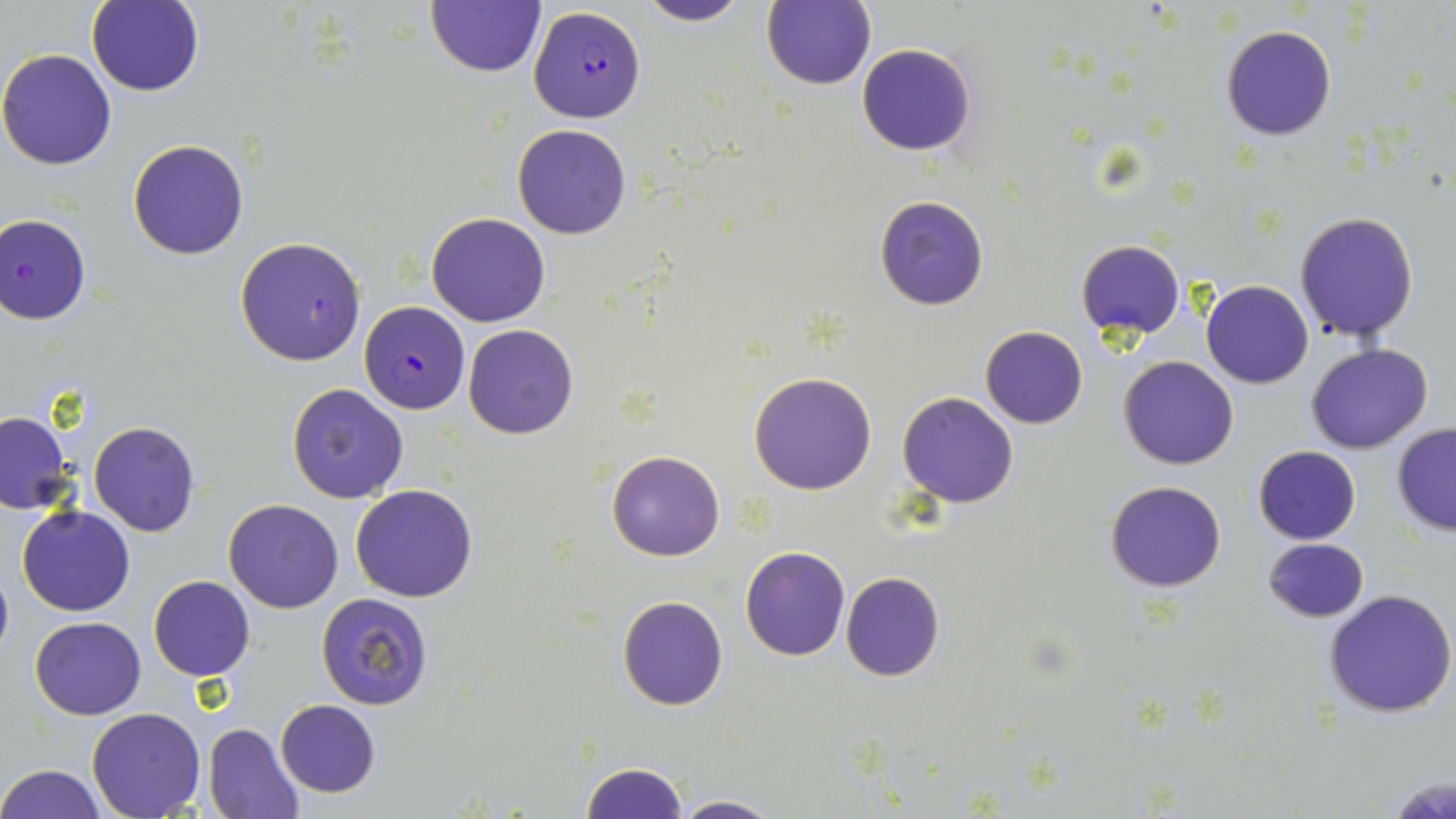

{
  "slide_level_diagnosis": "Plasmodium falciparum",
  "modality": "optical microscopy",
  "magnification": "1000x",
  "image_size": "1456×819 pixels",
  "preparation": "thin blood film",
  "plasmodium_falciparum_infected_red_blood_cell_locations": "approximate bounding boxes as [x1, y1, x2, y2] in pixels: [527, 5, 645, 124], [0, 213, 91, 323], [234, 236, 367, 367], [360, 300, 469, 412]",
  "uninfected_red_blood_cell_locations": "approximate bounding boxes as [x1, y1, x2, y2] in pixels: [86, 0, 205, 96], [636, 0, 753, 26], [424, 1, 545, 78], [760, 1, 876, 90], [1220, 24, 1337, 140], [856, 43, 978, 157], [0, 47, 119, 170], [512, 124, 632, 240], [128, 137, 251, 260], [874, 195, 990, 311], [1294, 210, 1420, 341], [427, 212, 548, 326], [1076, 240, 1186, 341], [1201, 280, 1314, 389], [463, 323, 579, 439], [980, 326, 1088, 429], [1306, 343, 1433, 455], [1118, 355, 1239, 470], [749, 371, 878, 495], [286, 384, 410, 503], [898, 392, 1019, 508], [0, 411, 73, 514], [88, 421, 201, 537], [1391, 423, 1456, 536], [1253, 446, 1360, 544], [607, 450, 725, 560], [1104, 479, 1227, 593], [350, 483, 479, 602], [224, 499, 344, 614], [18, 504, 135, 616], [1263, 537, 1369, 623], [740, 546, 851, 661], [0, 556, 13, 668], [840, 572, 945, 681], [149, 575, 255, 681], [1324, 589, 1455, 718], [315, 593, 434, 709], [616, 596, 729, 710], [30, 616, 145, 720], [276, 699, 381, 797], [87, 708, 206, 818], [203, 723, 306, 819], [579, 761, 688, 818], [0, 764, 106, 819], [1386, 772, 1456, 819], [670, 793, 781, 818]",
  "stain": "May-Grünwald-Giemsa",
  "field_of_view": "single"
}